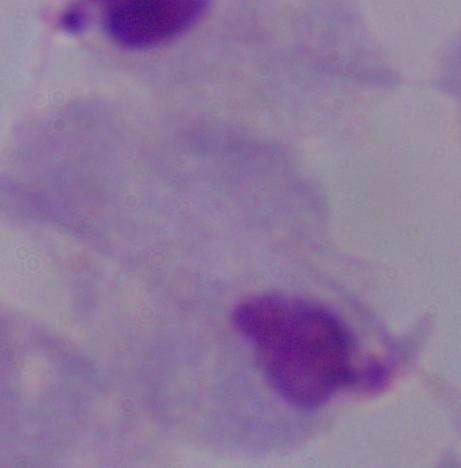

Summary:
  - Magnification: 1000x
  - Identification: trichomonad
  - Modality: photomicrograph